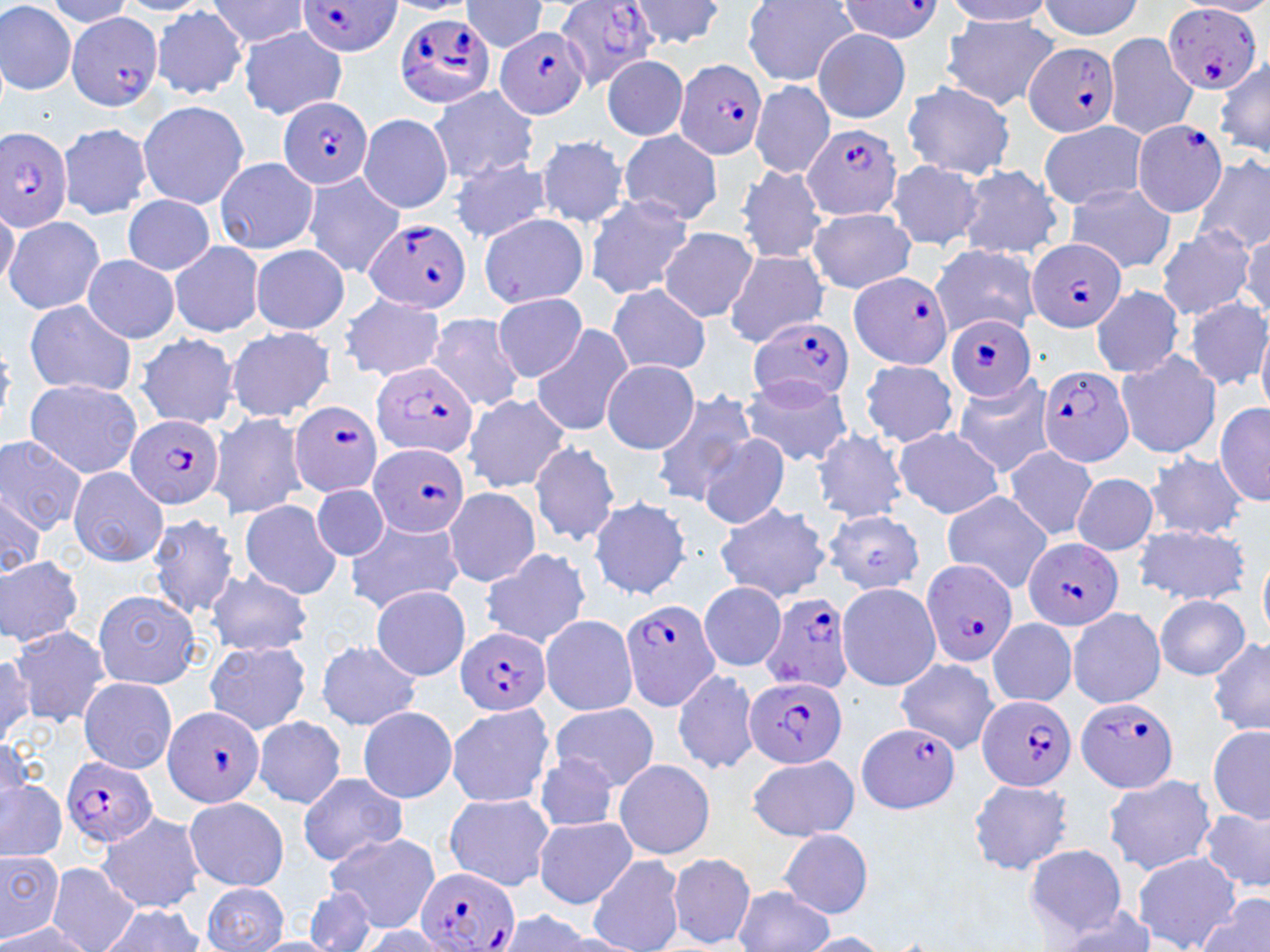
Summary:
  - Coordinate format: approximate bounding boxes as (x1,y1)-(x2,y2) corner pairs in pixels
  - Uninfected red blood cell locations: (41,0)-(139,28), (461,0)-(549,53), (625,0)-(726,50), (742,0)-(859,86), (944,0)-(1056,26), (114,1)-(213,16), (204,1)-(311,49), (381,1)-(469,15), (1037,1)-(1144,40), (1179,1)-(1270,18), (0,2)-(76,96), (152,7)-(250,99), (942,16)-(1059,110), (237,28)-(347,120), (812,29)-(911,123), (1103,32)-(1200,140), (601,55)-(689,141), (1216,58)-(1270,160), (750,79)-(834,179), (900,82)-(1016,180), (426,86)-(541,184), (136,100)-(250,209), (357,113)-(454,214), (1038,121)-(1150,210), (57,122)-(154,220), (618,130)-(723,227), (537,134)-(631,228), (450,155)-(552,244), (214,157)-(319,255), (1192,157)-(1270,255), (885,159)-(986,251), (955,164)-(1063,261), (735,165)-(829,264), (303,172)-(406,279), (1065,183)-(1177,274), (584,194)-(694,300), (122,195)-(215,274), (0,196)-(18,294), (806,206)-(917,293), (479,213)-(588,309), (4,215)-(107,316), (1238,225)-(1270,324), (659,227)-(757,322), (1155,227)-(1255,320), (169,241)-(265,337), (929,244)-(1043,336), (251,245)-(350,334), (724,250)-(829,347), (81,255)-(180,344), (608,284)-(711,376), (1090,284)-(1183,378), (494,293)-(585,381), (340,294)-(446,381), (1185,297)-(1270,392), (24,301)-(137,396), (424,314)-(527,412), (1256,322)-(1270,417), (531,323)-(636,439), (225,326)-(335,423), (134,333)-(239,428), (1115,350)-(1221,459), (602,359)-(700,452), (859,360)-(961,448), (951,373)-(1055,476), (739,374)-(854,467), (25,378)-(142,479), (649,388)-(758,505), (462,394)-(574,492), (1215,401)-(1268,507), (208,410)-(309,521), (891,426)-(1004,518), (813,429)-(911,521), (0,433)-(89,539), (697,434)-(790,529), (529,441)-(622,546), (1004,445)-(1098,541), (1145,452)-(1249,539), (68,465)-(169,568), (1072,472)-(1159,555), (312,485)-(389,562), (443,487)-(541,586), (0,490)-(50,582), (939,490)-(1055,593), (586,496)-(693,602), (238,498)-(344,598), (712,500)-(832,603), (820,509)-(926,594), (147,512)-(242,618), (345,517)-(464,612), (1133,524)-(1250,604), (1257,541)-(1269,643), (478,547)-(592,650), (0,555)-(84,647), (205,569)-(312,657), (698,580)-(787,672), (836,582)-(941,689), (370,585)-(471,681), (92,588)-(200,689), (1154,595)-(1251,680), (1067,607)-(1166,709), (540,615)-(639,715), (986,618)-(1077,707), (10,624)-(111,725), (1207,637)-(1270,736), (203,639)-(312,737), (316,640)-(422,731), (0,651)-(35,748), (895,657)-(1001,753), (671,667)-(760,776), (78,677)-(177,774), (549,702)-(659,792), (445,703)-(554,808), (356,706)-(457,804), (253,716)-(347,807), (1206,722)-(1270,824), (0,732)-(36,816), (526,751)-(624,829), (745,754)-(859,842), (612,759)-(716,861), (296,772)-(407,866), (1103,775)-(1216,874), (966,777)-(1076,876), (0,780)-(67,862), (443,792)-(553,891), (183,796)-(289,892), (1199,808)-(1269,893), (96,812)-(204,914), (532,817)-(636,908), (777,829)-(876,919), (325,832)-(440,933), (1023,843)-(1132,941), (0,849)-(62,942), (664,852)-(757,949), (1131,853)-(1240,950), (587,855)-(686,952), (44,863)-(140,952), (201,883)-(290,952), (304,885)-(380,952), (734,887)-(834,952), (1198,893)-(1270,952), (102,907)-(205,952), (1047,907)-(1163,950), (492,911)-(607,952), (1,919)-(92,951), (355,925)-(456,951), (797,932)-(895,951)
  - Plasmodium falciparum-infected red blood cell locations: (298,1)-(404,57), (555,2)-(661,85), (837,2)-(943,44), (1163,4)-(1261,94), (66,12)-(163,112), (393,13)-(494,108), (494,24)-(590,120), (1025,42)-(1119,137), (675,56)-(768,160), (279,96)-(372,190), (1131,120)-(1226,215), (803,123)-(900,220), (0,126)-(74,233), (364,217)-(472,314), (1026,238)-(1124,332), (848,271)-(953,369), (749,315)-(854,408), (945,315)-(1038,400), (370,361)-(478,458), (1042,367)-(1136,467), (290,401)-(384,497), (125,413)-(225,511), (370,442)-(468,538), (1024,536)-(1122,632), (920,557)-(1019,667), (759,592)-(855,693), (619,598)-(723,714), (457,626)-(551,717), (743,675)-(846,770), (977,693)-(1076,791), (1076,696)-(1180,795), (160,705)-(265,808), (856,721)-(962,815), (60,755)-(158,847), (416,867)-(520,952)
  - Slide-level diagnosis: Plasmodium falciparum
  - Image size: 1270×952 pixels
  - Modality: optical microscopy
  - Stain: May-Grünwald-Giemsa
  - Field of view: single
  - Preparation: thin blood film
  - Magnification: 1000x